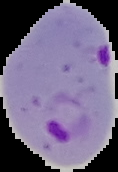

Result: Plasmodium parasites detected. Image is 118×172 pixels. Cell region segmented out of the field of view; the surrounding area is masked to black. From a thin blood smear.